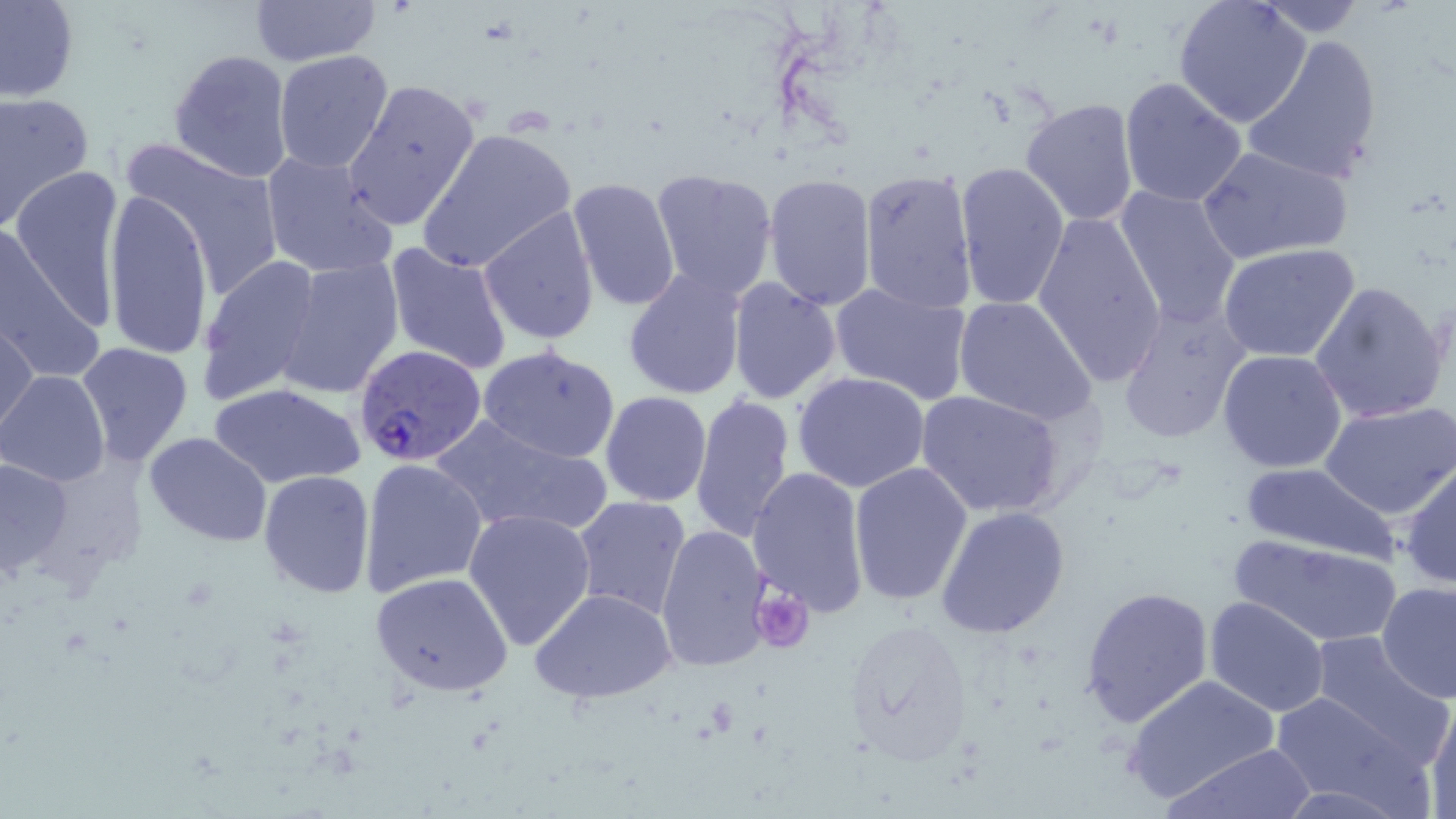
Summary:
  - Coordinate format: approximate bounding boxes as (x1, y1, x2, y2) in pixels
  - Uninfected red blood cell locations: (0, 0, 79, 103), (248, 0, 381, 69), (1173, 1, 1312, 127), (1252, 1, 1372, 36), (1243, 34, 1384, 186), (168, 48, 293, 183), (272, 48, 395, 174), (1119, 75, 1249, 208), (342, 78, 481, 232), (0, 90, 95, 231), (1022, 97, 1140, 226), (416, 127, 578, 274), (121, 137, 288, 301), (1197, 143, 1354, 265), (259, 148, 399, 280), (953, 161, 1071, 309), (9, 164, 128, 331), (859, 167, 980, 313), (650, 168, 780, 301), (762, 174, 877, 311), (566, 176, 682, 314), (1113, 185, 1242, 327), (102, 188, 216, 361), (478, 206, 600, 347), (1030, 209, 1168, 386), (0, 229, 100, 381), (382, 241, 515, 373), (1217, 243, 1362, 363), (198, 254, 325, 405), (276, 259, 405, 399), (622, 268, 747, 400), (727, 276, 842, 403), (828, 280, 973, 404), (1309, 280, 1451, 425), (953, 295, 1097, 426), (1117, 300, 1253, 444), (1, 322, 38, 442), (0, 340, 64, 470), (75, 342, 194, 467), (478, 344, 621, 463), (1217, 349, 1348, 474), (0, 370, 109, 487), (791, 372, 931, 494), (208, 382, 365, 490), (916, 389, 1067, 518), (600, 392, 712, 507), (689, 392, 798, 545), (1322, 399, 1456, 519), (430, 414, 611, 536), (143, 431, 273, 546), (0, 454, 79, 581), (358, 457, 489, 600), (848, 461, 975, 607), (1400, 461, 1456, 588), (1239, 462, 1399, 563), (748, 468, 872, 618), (259, 470, 376, 597), (570, 495, 693, 621), (935, 506, 1070, 638), (465, 509, 598, 652), (656, 523, 773, 673), (1232, 534, 1403, 648), (371, 571, 514, 698), (1376, 580, 1456, 702), (1080, 585, 1216, 729), (529, 588, 678, 706), (1205, 597, 1330, 717), (841, 618, 974, 766), (1304, 629, 1451, 764), (1121, 674, 1281, 808), (1268, 689, 1425, 812), (1424, 695, 1456, 817), (1165, 744, 1318, 818)
  - Plasmodium falciparum-infected red blood cell locations: (355, 344, 489, 466)
  - Platelet locations: (754, 590, 814, 653)
  - Slide-level diagnosis: Plasmodium falciparum
  - Preparation: thin blood film
  - Image size: 1456×819 pixels
  - Field of view: one of a larger specimen
  - Stain: May-Grünwald-Giemsa
  - Modality: optical microscopy
  - Magnification: 1000x